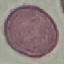
result = no malaria parasites detected
capture = smartphone through the microscope eyepiece
image type = cell patch, automatically extracted from a larger field of view and resized to 64 × 64 pixels
preparation = thin blood smear
stain = Giemsa